Identify the parasite.
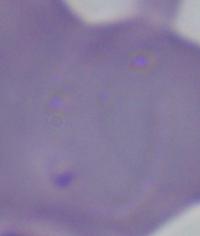

This is Babesia.

Micrograph. 1000x magnification.